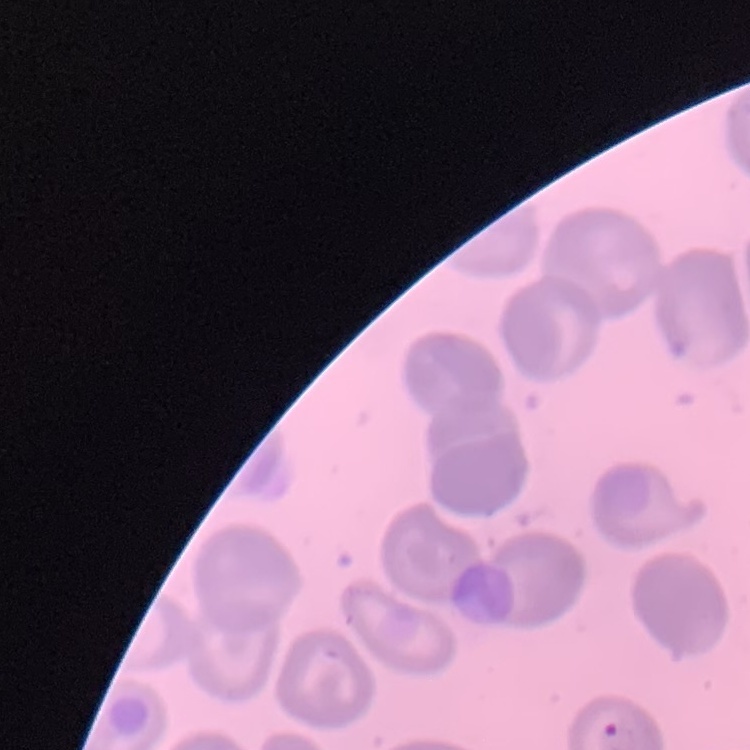
Summary:
  - Red blood cell morphology: no rouleaux formation
  - Image type: square crop of a larger photomicrograph
  - Preparation: thin blood film
  - Stain: Field's or Giemsa